Classify this cell by malaria status.
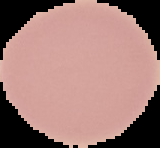
Uninfected.

{
  "image_size": "160×148 pixels",
  "preparation": "thin blood smear",
  "image_type": "segmented cell region with the area outside set to black"
}